Comment on the morphology of the erythrocytes.
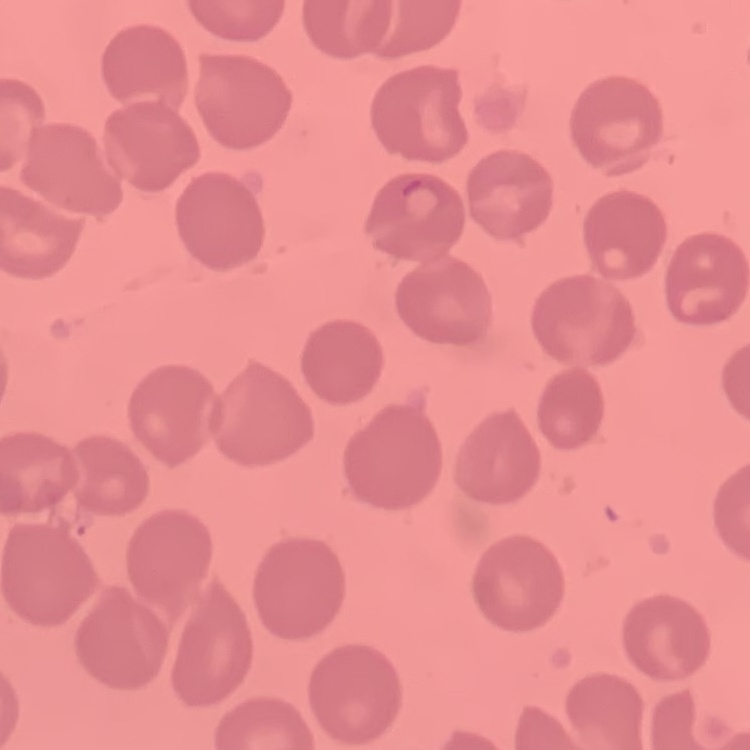
They show no rouleaux formation.

Summary:
  - Image type: one tile cut from a larger photomicrograph
  - Stain: Field's or Giemsa
  - Preparation: thin blood smear